Assess this cell for malaria.
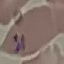

It is parasitized.

Acquired by smartphone through the microscope eyepiece. Automatically extracted cell patch, resized to 64 × 64 pixels. Giemsa-stained preparation. Thin blood smear.